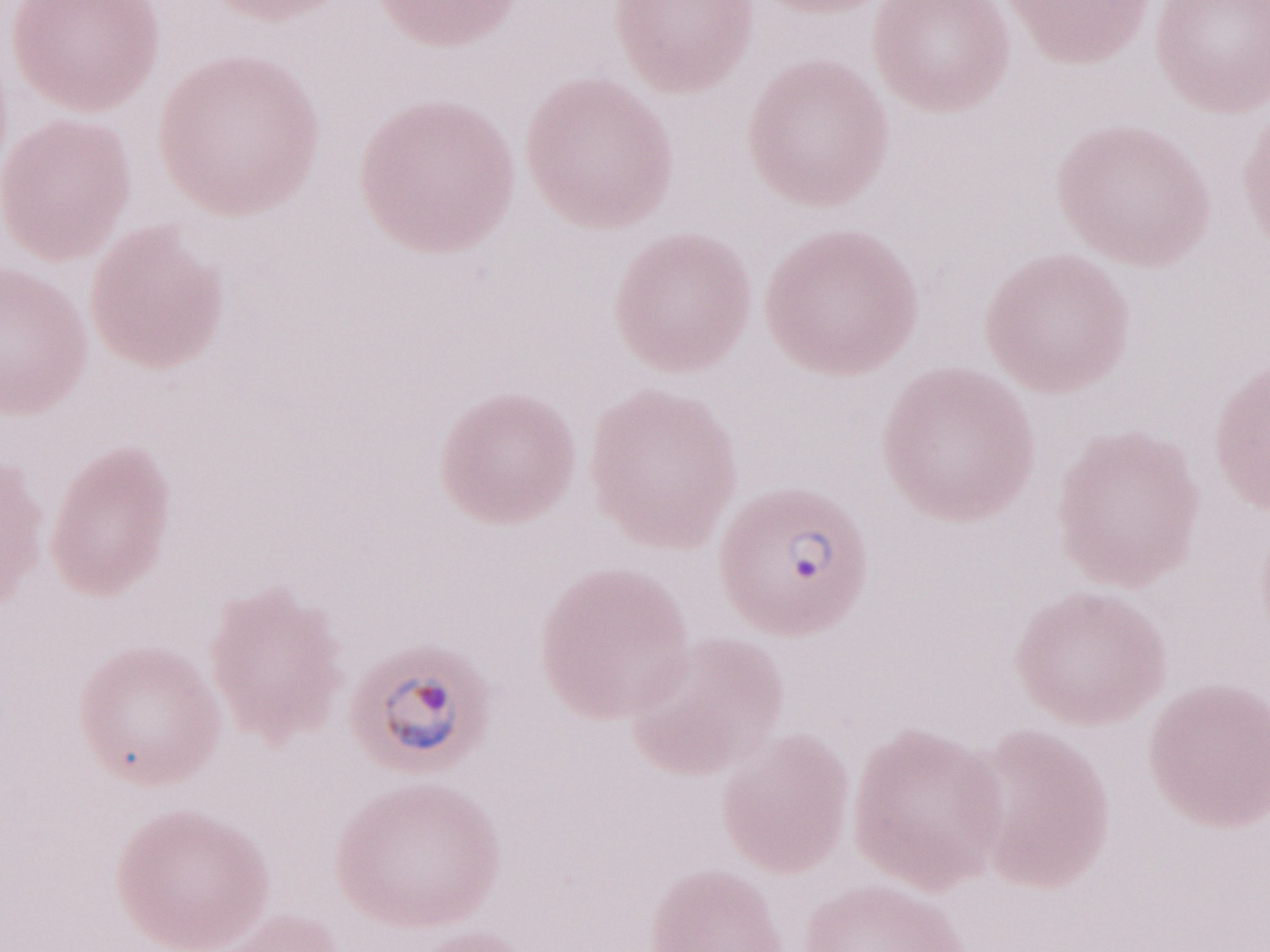 1,000x magnification. Patient-level malaria diagnosis: positive. Thin peripheral-blood smear. Image is 1270×952 pixels. May-Grünwald-Giemsa stain. Olympus BX43 microscope, Olympus DP73 camera. One field of this slide.